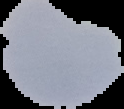
image type = segmented cell region with the area outside set to black
image size = 124×109 pixels
preparation = thin blood film
malaria status = parasitized